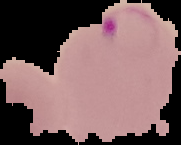
Malaria status: parasitized. From a thin blood smear. Image is 181×145 pixels. Cell region segmented out of the field of view; the surrounding area is masked to black.